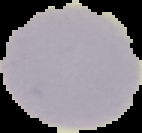
Image is 142×133 pixels. Malaria status: uninfected. From a thin blood smear. The area outside the segmented cell region is set to black.